Outline every leukocyte.
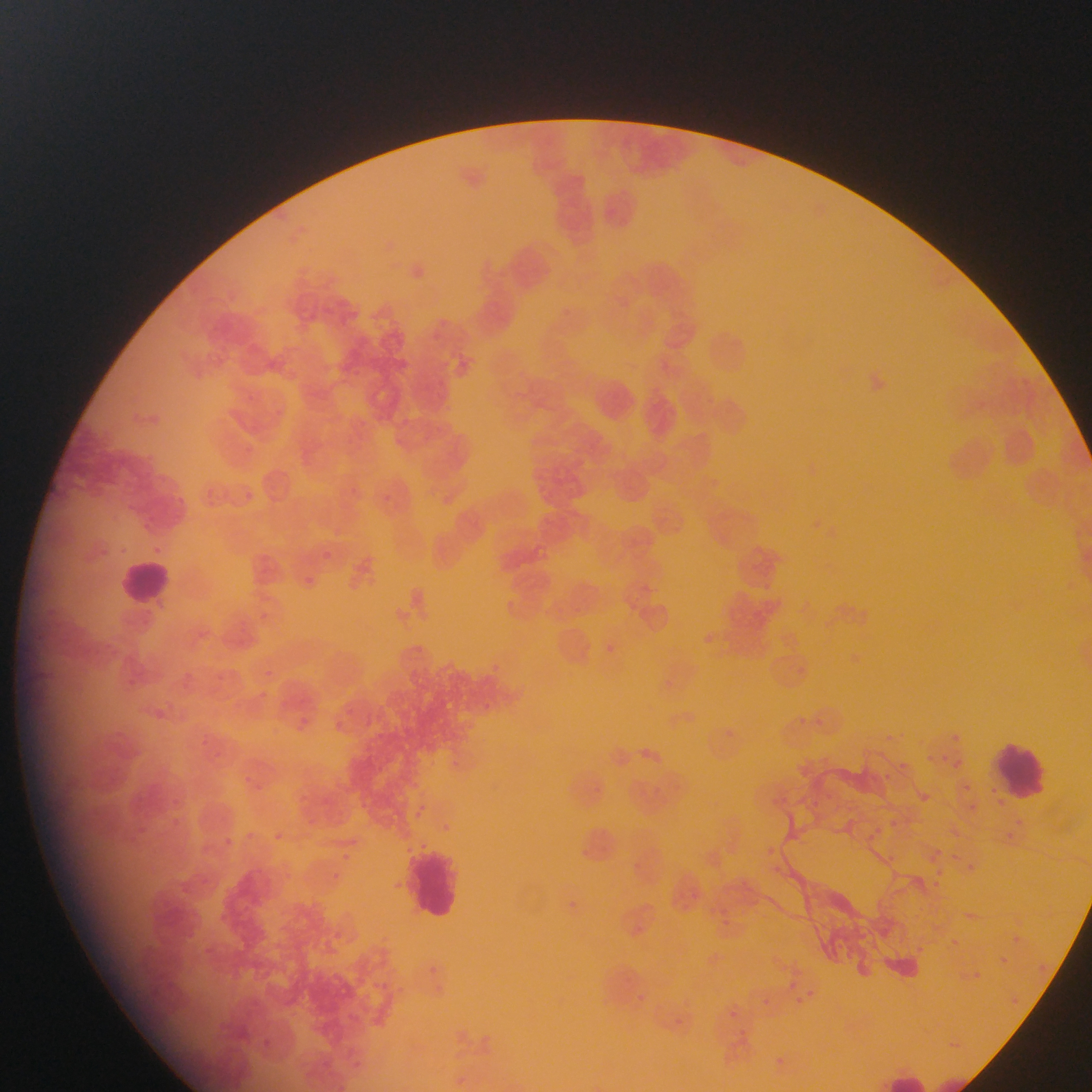

Approximate bounding boxes as (left, top, right, bottom) in pixels.
Leukocytes: (118, 553, 176, 612), (990, 740, 1054, 803), (405, 845, 467, 922), (877, 1067, 930, 1092).

Malaria parasite locations: (433, 374, 447, 389), (400, 414, 414, 431), (345, 482, 359, 498), (244, 485, 259, 505), (315, 543, 341, 564), (302, 565, 318, 584), (489, 656, 501, 668), (262, 662, 280, 679), (254, 684, 272, 703), (291, 713, 325, 745), (817, 713, 827, 728), (798, 714, 812, 727), (334, 716, 347, 728), (948, 733, 976, 747), (199, 734, 207, 744), (943, 748, 956, 766), (929, 754, 942, 766), (429, 755, 447, 772), (954, 756, 981, 778), (902, 758, 916, 774), (884, 767, 905, 785), (246, 772, 260, 784), (412, 777, 422, 782), (962, 783, 974, 800), (298, 791, 310, 800), (168, 796, 193, 810), (412, 800, 433, 822), (173, 816, 190, 833), (1011, 816, 1028, 829), (887, 818, 901, 828), (997, 818, 1014, 852), (869, 820, 884, 833), (269, 825, 285, 846), (221, 829, 244, 848), (867, 829, 875, 847), (767, 843, 775, 854), (927, 850, 946, 862), (338, 852, 348, 858), (887, 854, 904, 865), (963, 858, 981, 877), (774, 863, 788, 878), (934, 863, 948, 882), (333, 873, 343, 888), (934, 878, 946, 894), (563, 896, 590, 915), (677, 898, 690, 913), (721, 913, 735, 925), (1008, 931, 1025, 947), (947, 936, 959, 948), (913, 939, 930, 956), (995, 953, 1011, 968), (1035, 962, 1055, 976), (419, 964, 445, 978), (969, 968, 984, 982), (379, 975, 396, 990), (784, 977, 797, 990), (801, 984, 815, 996), (760, 995, 768, 1006), (790, 999, 807, 1010), (730, 1008, 741, 1020), (264, 1033, 276, 1048), (320, 1057, 336, 1067), (774, 1058, 790, 1069), (355, 1059, 364, 1066). Collected in Ghana. Thin blood film. One field of view. Photographed through a microscope with a mobile-phone camera. Image is 1092×1092 pixels.